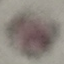
Malaria status: uninfected. Thin blood smear. Giemsa stain. Automatically extracted cell patch, resized to 64 × 64 pixels. Photographed with a smartphone camera at the microscope eyepiece.